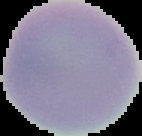
image size = 142×136 pixels
image type = segmented cell region with the area outside set to black
preparation = thin blood smear
malaria status = uninfected